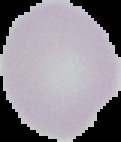

result: no Plasmodium parasites detected
image_size: 121×142 pixels
image_type: segmented cell region on a black background
preparation: thin blood film